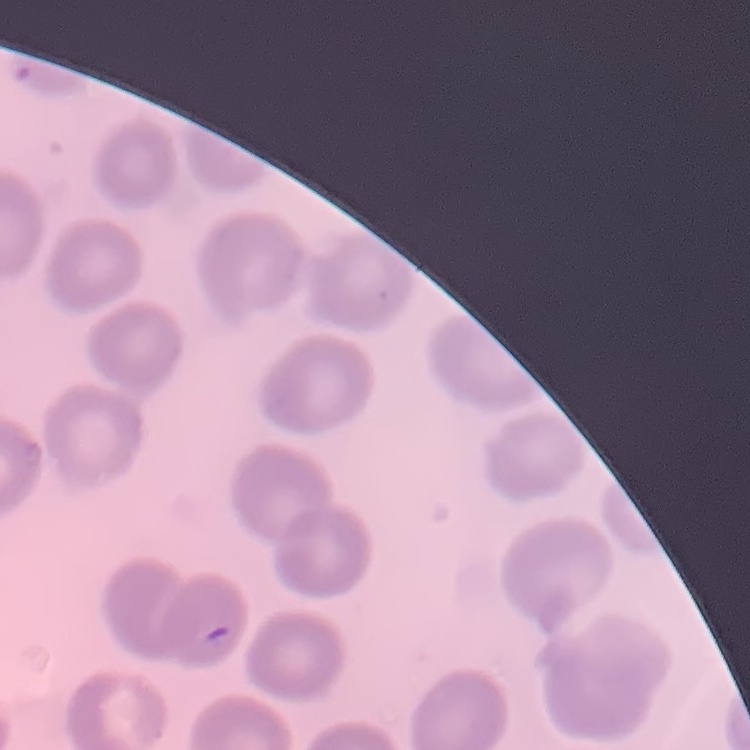

{
  "erythrocyte_morphology": "no rouleaux formation",
  "stain": "Field's or Giemsa",
  "image_type": "one tile cut from a larger photomicrograph",
  "preparation": "thin blood film"
}